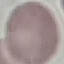 Result: no malaria parasites seen. Thin blood film. Giemsa stain. Automatically extracted cell patch, resized to 64 × 64 pixels. Photographed with a smartphone camera at the microscope eyepiece.